Point out every malaria parasite.
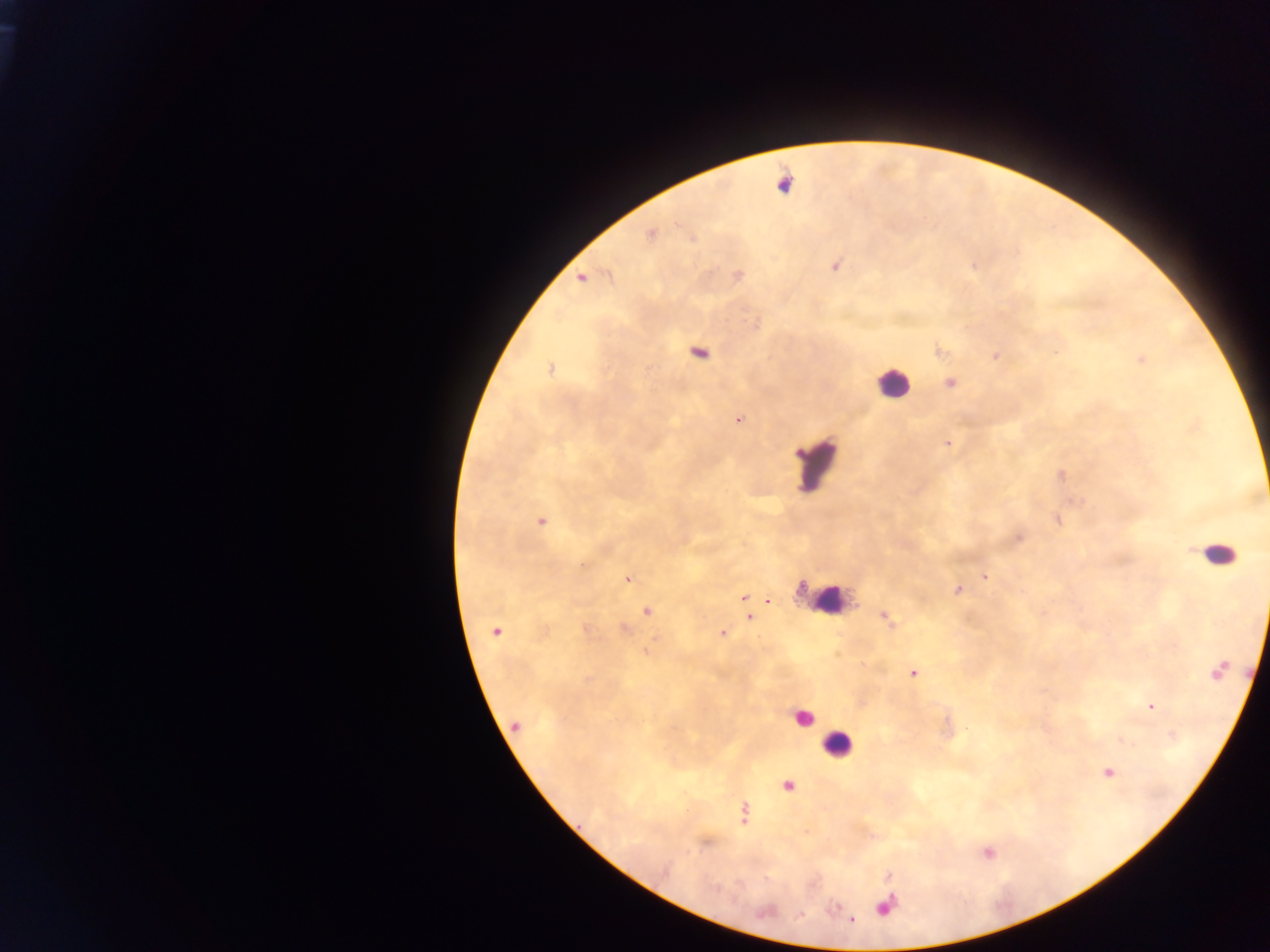
Approximate centers as {x, y} in pixels.
Malaria parasites: {651, 234}, {692, 239}, {836, 266}, {738, 276}, {581, 277}, {699, 354}, {995, 356}, {1142, 359}, {550, 369}, {951, 383}, {737, 420}, {947, 444}, {1058, 520}, {541, 522}, {1019, 538}, {583, 564}, {985, 577}, {628, 579}, {957, 591}, {744, 597}, {768, 601}, {648, 611}, {749, 617}, {885, 617}, {624, 629}, {494, 632}, {722, 633}, {913, 673}, {1150, 707}, {516, 726}, {1108, 771}, {788, 786}, {744, 813}, {885, 907}.

Summary:
  - Leukocyte locations: {891, 383}, {818, 466}, {1218, 553}, {827, 599}, {804, 718}, {837, 744}
  - Preparation: thick blood smear
  - Field of view: single
  - Image size: 1270×952 pixels
  - Country: Ghana
  - Capture: mobile-phone photograph through a microscope